Identify the parasite.
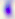

Toxoplasma gondii.

modality = micrograph
magnification = 400x